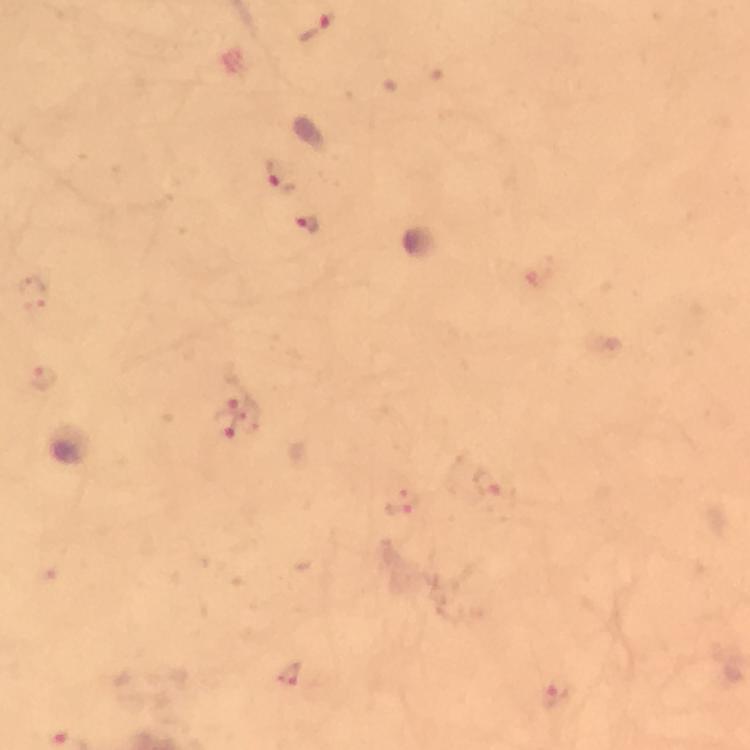

Approximate centers as [x, y] in pixels.
Summary:
  - Plasmodium parasite locations: [317, 27], [279, 174], [312, 227], [32, 295], [43, 378], [231, 388], [228, 424], [488, 482], [404, 501], [289, 673], [555, 694]
  - Image size: 750×750 pixels
  - Preparation: thick blood smear
  - Immersion oil: applied
  - Context: from a malaria diagnostic workup
  - Cropped from: one field of view
  - Stain: Giemsa
  - Capture: smartphone photograph through a microscope
  - Magnification: 100x